Report the malaria status of this cell.
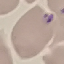

It is uninfected.

Acquired by smartphone through the microscope eyepiece. Cell patch, automatically extracted from a larger field of view and resized to 64 × 64 pixels. Giemsa stain. Thin smear of blood.